Classify this cell by malaria status.
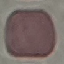
Uninfected.

Acquired by smartphone through the microscope eyepiece. Thin blood film. Automatically extracted cell patch, resized to 64 × 64 pixels. Giemsa-stained preparation.